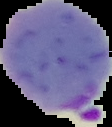
From a thin blood smear. Image is 112×127 pixels. The area outside the segmented cell region is set to black. Malaria status: parasitized.